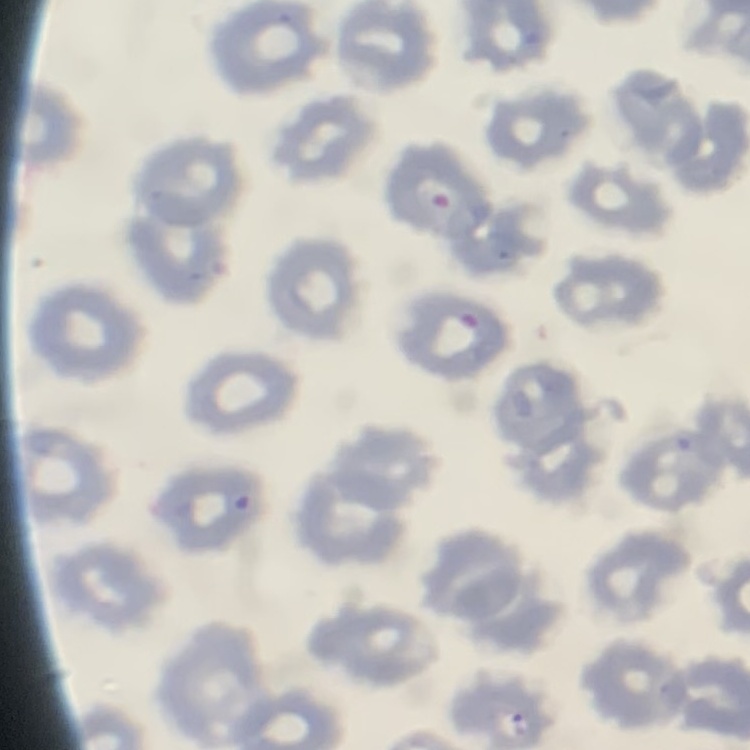
red_blood_cell_morphology: no rouleaux formation
stain: Field's or Giemsa
preparation: thin blood smear
image_type: one tile cut from a larger photomicrograph